Assess this cell for malaria.
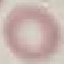

It is uninfected.

capture = smartphone through the microscope eyepiece
preparation = thin blood film
image type = automatically extracted cell patch, resized to 64 × 64 pixels
stain = Giemsa